Identify the cell.
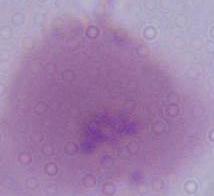

An erythrocyte.

Micrograph. 1000x magnification.